Outline each Plasmodium ovale-infected red blood cell.
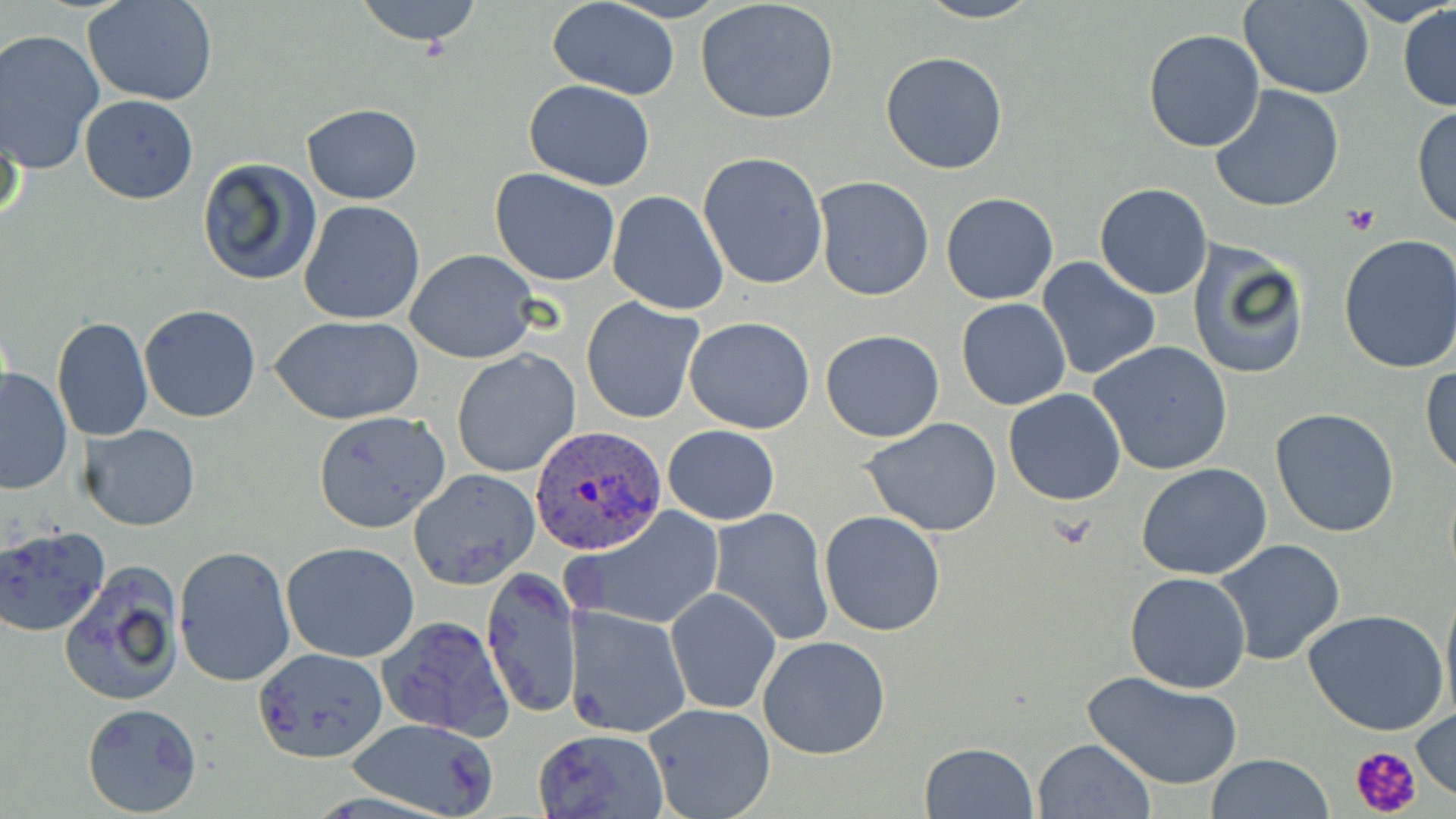

Approximate bounding boxes as (x1, y1, x2, y2) in pixels.
Plasmodium ovale-infected red blood cells: (531, 426, 665, 554).

slide-level diagnosis = Plasmodium ovale
platelet locations = approximate bounding boxes as (x1, y1, x2, y2) in pixels: (1341, 205, 1382, 235), (1350, 744, 1424, 817)
preparation = thin blood smear
stain = May-Grünwald-Giemsa
magnification = 1000x
image size = 1456×819 pixels
modality = light microscopy
field of view = one of a larger specimen
uninfected red blood cell locations = approximate bounding boxes as (x1, y1, x2, y2) in pixels: (84, 0, 220, 106), (352, 0, 488, 51), (547, 0, 681, 98), (914, 0, 1045, 23), (1239, 0, 1373, 99), (1345, 0, 1455, 27), (695, 1, 842, 124), (1397, 3, 1456, 112), (1143, 28, 1267, 153), (0, 29, 104, 174), (879, 52, 1009, 176), (523, 80, 656, 190), (1210, 85, 1346, 214), (80, 94, 198, 204), (300, 103, 422, 203), (1412, 104, 1456, 231), (0, 110, 24, 233), (697, 151, 829, 290), (196, 157, 323, 287), (490, 169, 620, 285), (812, 176, 934, 302), (1094, 183, 1213, 299), (605, 190, 729, 315), (941, 192, 1059, 306), (297, 199, 425, 326), (1335, 234, 1456, 376), (1187, 240, 1312, 381), (406, 248, 539, 364), (1037, 257, 1162, 379), (581, 296, 705, 424), (955, 298, 1072, 411), (138, 305, 262, 423), (268, 315, 424, 424), (52, 317, 154, 442), (685, 317, 816, 433), (819, 330, 945, 442), (1088, 340, 1233, 475), (451, 349, 581, 479), (1421, 363, 1455, 479), (0, 367, 73, 494), (1004, 389, 1127, 507), (1270, 407, 1400, 539), (313, 411, 453, 535), (860, 418, 1005, 537), (80, 423, 200, 531), (664, 424, 779, 526), (1136, 462, 1273, 581), (407, 467, 541, 589), (566, 506, 724, 632), (710, 508, 835, 646), (820, 511, 946, 637), (0, 526, 110, 639), (1213, 538, 1346, 667), (281, 542, 422, 663), (174, 545, 296, 690), (59, 563, 184, 708), (480, 566, 580, 720), (1124, 572, 1252, 695), (1440, 578, 1456, 723), (665, 586, 781, 715), (564, 605, 691, 740), (1303, 609, 1449, 737), (377, 614, 515, 742), (757, 635, 891, 759), (252, 648, 387, 763), (1082, 670, 1245, 790), (81, 702, 203, 817), (644, 703, 776, 819), (1413, 705, 1455, 799), (346, 717, 502, 817), (532, 727, 671, 819), (1033, 738, 1156, 818), (919, 742, 1038, 818), (1205, 755, 1336, 817)